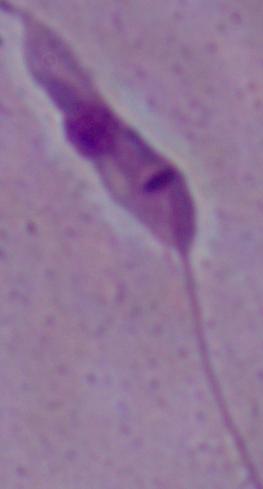

Micrograph. Captured at 1000x magnification. A Leishmania parasite is seen.